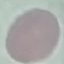

Summary:
  - Malaria status: uninfected
  - Preparation: thin blood film
  - Capture: smartphone through the microscope eyepiece
  - Image type: automatically extracted cell patch, resized to 64 × 64 pixels
  - Stain: Giemsa